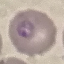
malaria_status: parasitized
preparation: thin smear
image_type: cell patch, automatically extracted from a larger field of view and resized to 64 × 64 pixels
stain: Giemsa
capture: smartphone camera at the microscope eyepiece